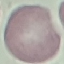
Summary:
  - Result: negative for malaria parasites
  - Stain: Giemsa
  - Image type: cell patch, automatically extracted from a larger field of view and resized to 64 × 64 pixels
  - Capture: smartphone through the microscope eyepiece
  - Preparation: thin blood film